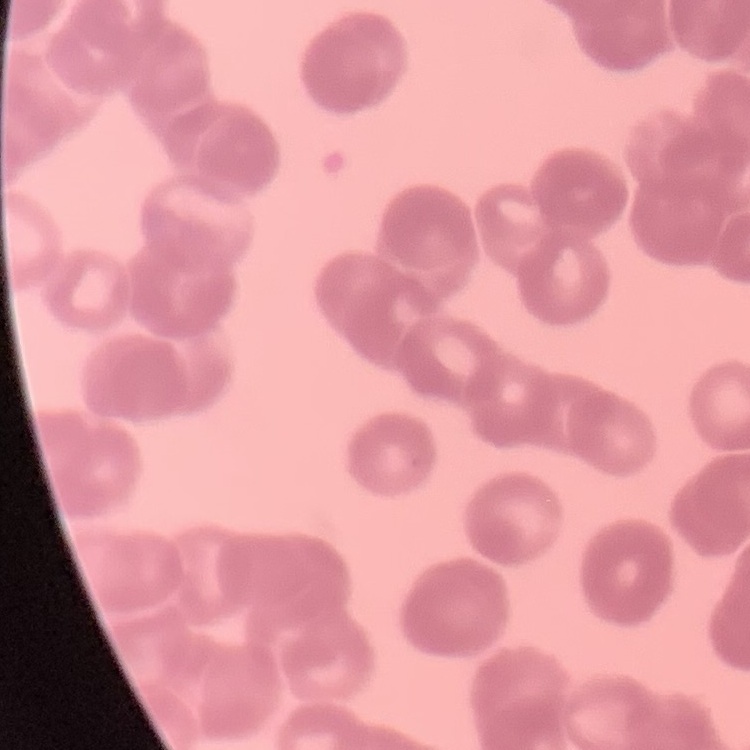
Summary:
  - Red blood cell morphology: rouleaux formation
  - Stain: Field's or Giemsa
  - Preparation: thin blood smear
  - Image type: one tile cut from a larger photomicrograph